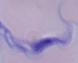
identification = trypanosome
modality = micrograph
magnification = 1000x